Classify this cell by malaria status.
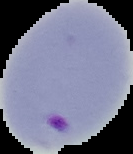
It is parasitized.

Image is 133×154 pixels. The area outside the segmented cell region is set to black. From a thin blood film.